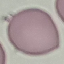

{
  "result": "negative for malaria parasites",
  "capture": "smartphone camera at the microscope eyepiece",
  "image_type": "cell patch, automatically extracted from a larger field of view and resized to 64 × 64 pixels",
  "preparation": "thin blood smear",
  "stain": "Giemsa"
}